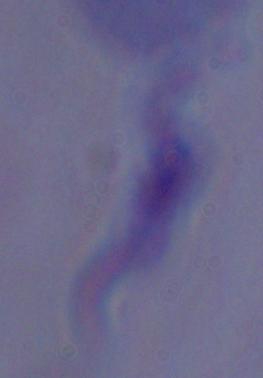 A trypanosome is seen. Micrograph. 1000x magnification.